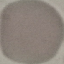

Summary:
  - Malaria status: uninfected
  - Preparation: thin smear
  - Stain: Giemsa
  - Capture: smartphone camera at the microscope eyepiece
  - Image type: cell patch, automatically extracted from a larger field of view and resized to 64 × 64 pixels